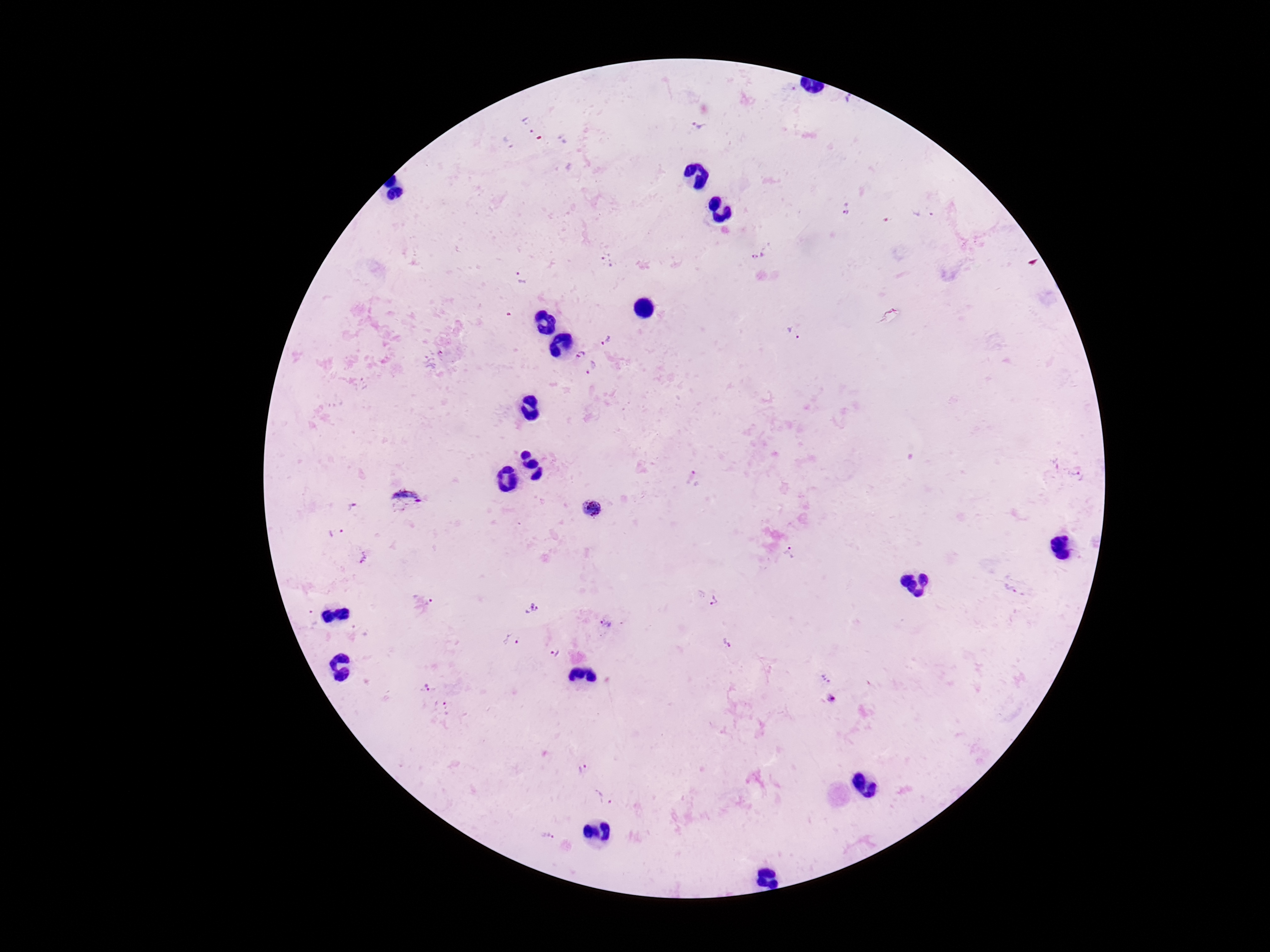
Approximate centers as [x, y] in pixels.
Summary:
  - Plasmodium parasite locations: [846, 101], [529, 124], [700, 124], [507, 142], [846, 209], [759, 256], [609, 259], [522, 278], [794, 333], [605, 342], [579, 353], [592, 367], [1077, 476], [693, 479], [406, 502], [592, 507], [354, 508], [337, 533], [787, 552], [363, 557], [1012, 589], [711, 599], [424, 605], [531, 608], [605, 624], [511, 641], [727, 643], [555, 653], [825, 677], [427, 686], [831, 699], [443, 709], [581, 768], [605, 798], [549, 836]
  - Capture: smartphone camera through the microscope eyepiece
  - Image size: 1270×952 pixels
  - Magnification: 100x
  - Stain: Giemsa
  - Patient malaria status: infected
  - Field of view: one from this slide
  - Preparation: thick blood smear